Locate every uninfected red blood cell.
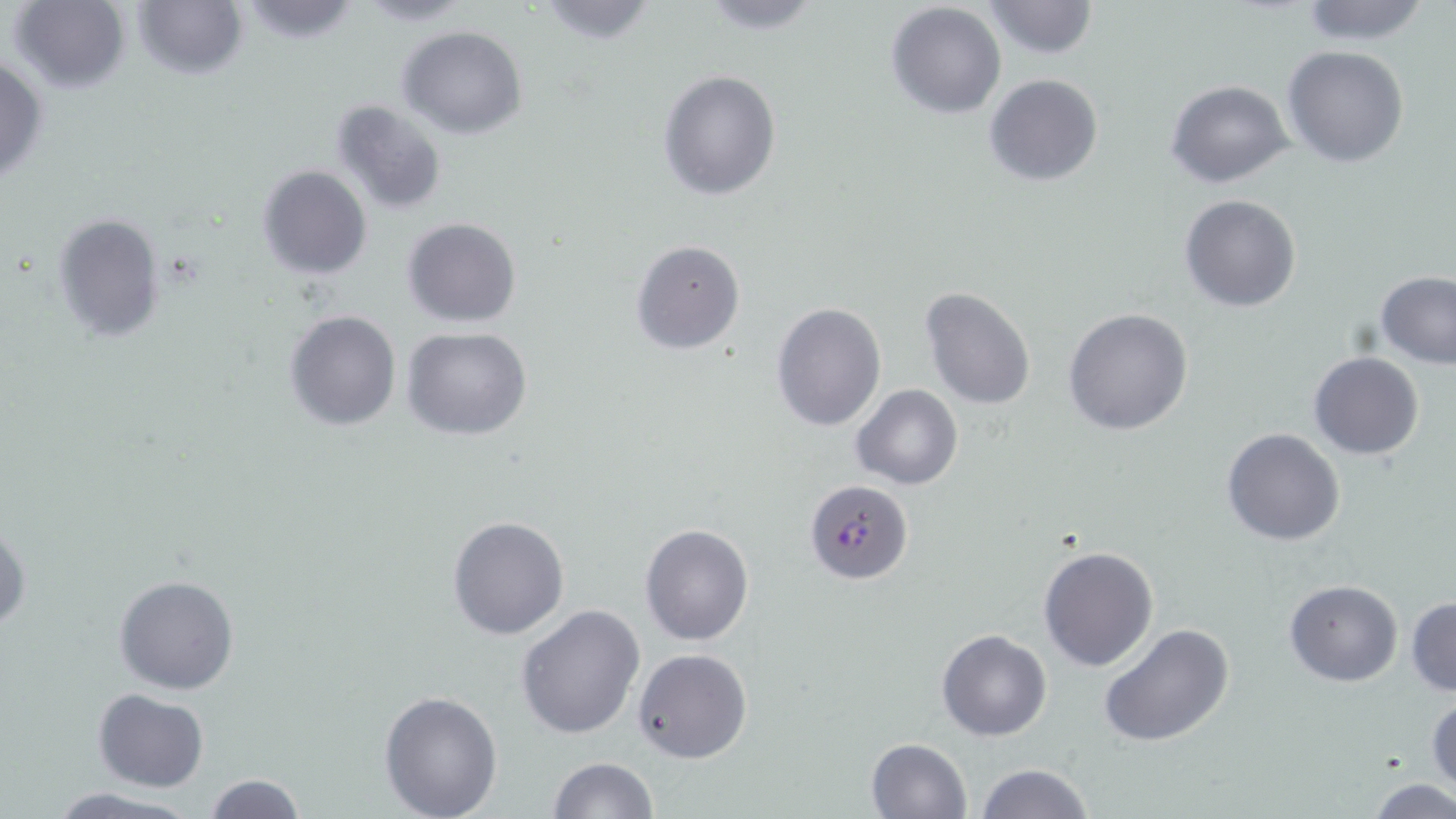
Approximate bounding boxes as [x1, y1, x2, y2] in pixels.
Uninfected red blood cells: [8, 0, 129, 94], [133, 0, 247, 80], [531, 0, 660, 46], [690, 0, 828, 35], [1297, 0, 1433, 44], [354, 1, 476, 25], [980, 1, 1098, 59], [236, 2, 364, 47], [885, 3, 1007, 119], [397, 25, 528, 139], [1282, 45, 1408, 168], [0, 53, 50, 185], [658, 69, 782, 200], [984, 73, 1104, 186], [1166, 80, 1293, 187], [329, 99, 449, 215], [257, 166, 372, 280], [1179, 194, 1301, 312], [51, 213, 166, 343], [401, 216, 522, 328], [630, 239, 745, 355], [1376, 272, 1456, 368], [919, 286, 1036, 409], [770, 301, 887, 433], [1062, 306, 1196, 436], [284, 311, 401, 430], [402, 327, 533, 442], [1307, 351, 1426, 459], [851, 384, 962, 490], [1222, 429, 1346, 547], [447, 514, 570, 640], [0, 519, 30, 634], [639, 523, 754, 645], [1038, 544, 1159, 670], [113, 573, 239, 696], [1283, 579, 1403, 686], [1405, 596, 1456, 697], [514, 604, 645, 741], [1098, 622, 1235, 748], [937, 629, 1052, 741], [633, 647, 753, 764], [93, 689, 208, 792], [378, 690, 504, 819], [1428, 691, 1456, 794], [866, 737, 973, 819], [547, 757, 656, 819], [974, 763, 1092, 819], [202, 775, 308, 818], [1369, 778, 1455, 818], [46, 787, 197, 819].

Plasmodium falciparum-infected red blood cell locations = approximate bounding boxes as [x1, y1, x2, y2] in pixels: [803, 479, 912, 584]
slide-level diagnosis = Plasmodium falciparum
image size = 1456×819 pixels
preparation = thin blood film
stain = May-Grünwald-Giemsa
field of view = single
modality = light microscopy
magnification = 1000x